Identify the cell.
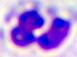

This is a leukocyte.

Summary:
  - Magnification: 400x
  - Modality: photomicrograph